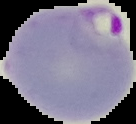 The area outside the segmented cell region is set to black. Image is 136×124 pixels. From a thin blood smear. Result: Plasmodium parasites detected.